Classify this cell by malaria status.
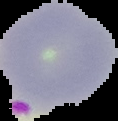

It is parasitized.

{
  "preparation": "thin blood smear",
  "image_type": "segmented cell region on a black background",
  "image_size": "118×121 pixels"
}